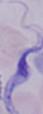

Summary:
  - Magnification: 1000x
  - Identification: trypanosome
  - Modality: micrograph